State which parasite is depicted.
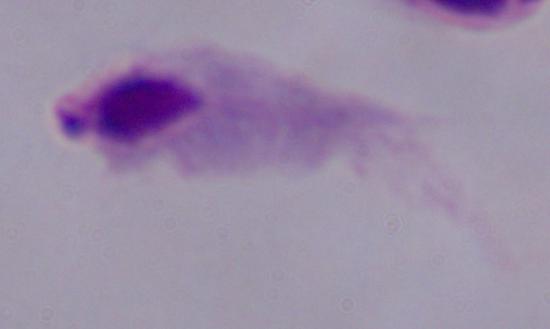

A trichomonad.

magnification = 1000x
modality = micrograph